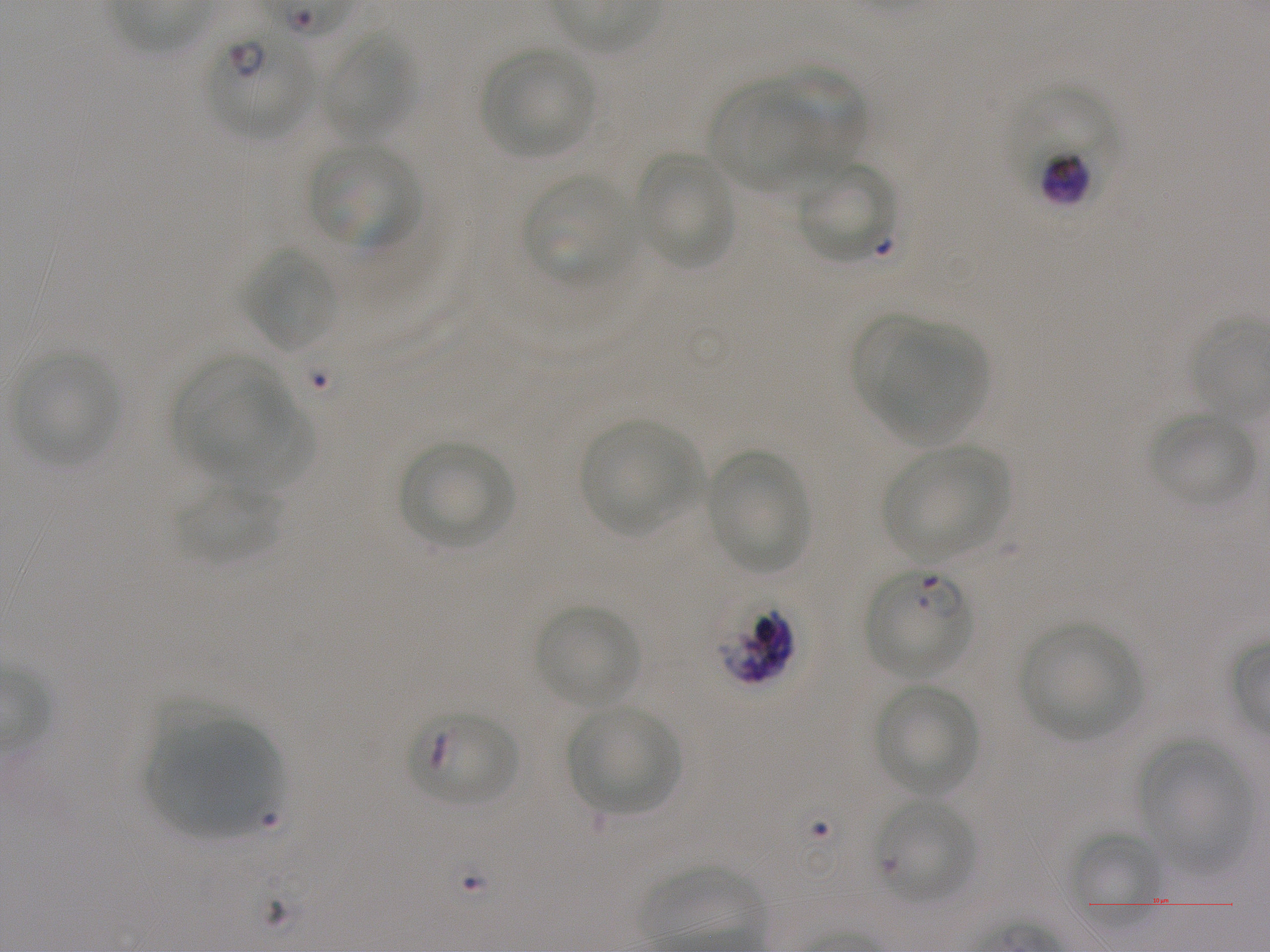

Not every red blood cell is marked. A life-cycle stage — or a range of stages, where the recorded stages span more than one — follows each staged infected red blood cell.
{
  "donor_blood_group": "A+",
  "preparation": "thin blood film",
  "objective": "100x, oil immersion, numerical aperture 1.25",
  "locations_of_infected_red_blood_cells": "approximate bounding boxes as (x1, y1, x2, y2) in pixels: (208, 33, 313, 140) early ring to early trophozoite; (1007, 82, 1118, 203) early trophozoite to early schizont; (863, 569, 974, 679) ring; (715, 596, 797, 685) late trophozoite to late schizont; (406, 714, 517, 802) late ring",
  "locations_of_uninfected_red_blood_cells": "approximate bounding boxes as (x1, y1, x2, y2) in pixels: (322, 34, 415, 140), (482, 49, 595, 159), (771, 63, 866, 170), (708, 81, 818, 189), (309, 143, 421, 250), (635, 152, 735, 270), (800, 161, 898, 265), (522, 176, 636, 283), (242, 246, 339, 353), (850, 313, 938, 423), (877, 321, 985, 445), (11, 352, 120, 467), (174, 356, 289, 475), (193, 390, 315, 494), (1148, 412, 1256, 507), (579, 419, 704, 536), (399, 442, 515, 549), (883, 447, 1008, 561), (705, 450, 809, 574), (176, 482, 281, 564), (535, 604, 639, 709), (1019, 623, 1142, 739), (874, 684, 980, 797), (567, 705, 681, 814), (143, 720, 278, 838), (1139, 739, 1250, 875), (1071, 832, 1161, 925)",
  "locations_of_red_blood_cells_of_indeterminate_infection_status": "approximate bounding boxes as (x1, y1, x2, y2) in pixels: (874, 798, 976, 906)",
  "field_of_view": "single",
  "stain": "Giemsa",
  "culture": "in-vitro P. falciparum strain NF54, static",
  "image_size": "1270×952 pixels"
}